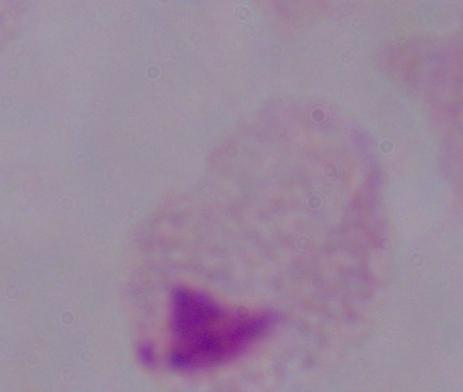
magnification = 1000x
identification = trichomonad
modality = photomicrograph